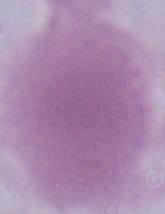
magnification = 1000x
modality = micrograph
identification = red blood cell